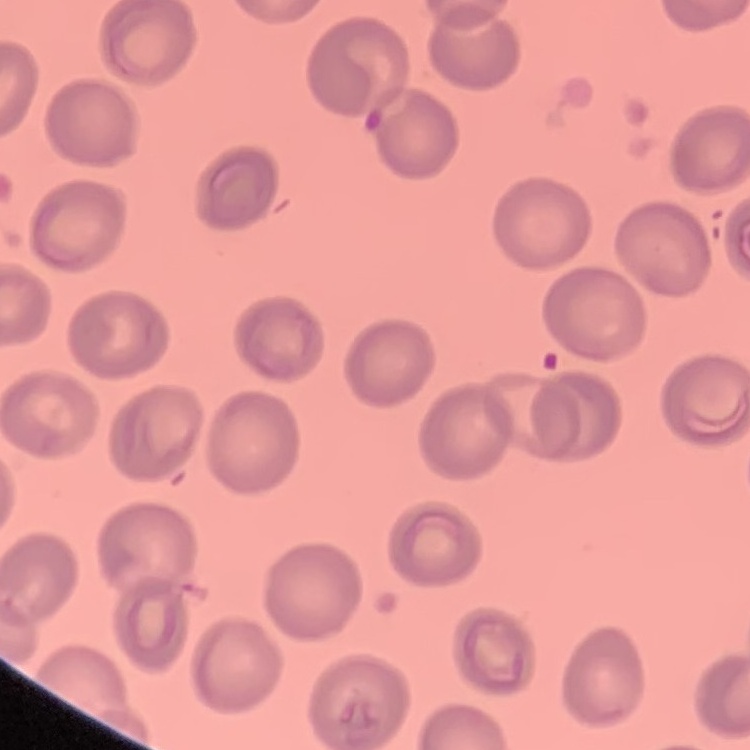

Summary:
  - Red blood cell morphology: no rouleaux formation
  - Stain: Field's or Giemsa
  - Image type: square crop of a larger photomicrograph
  - Preparation: thin peripheral smear